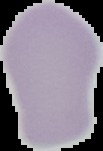
The area outside the segmented cell region is set to black. Image is 103×151 pixels. From a thin blood smear. Malaria status: uninfected.